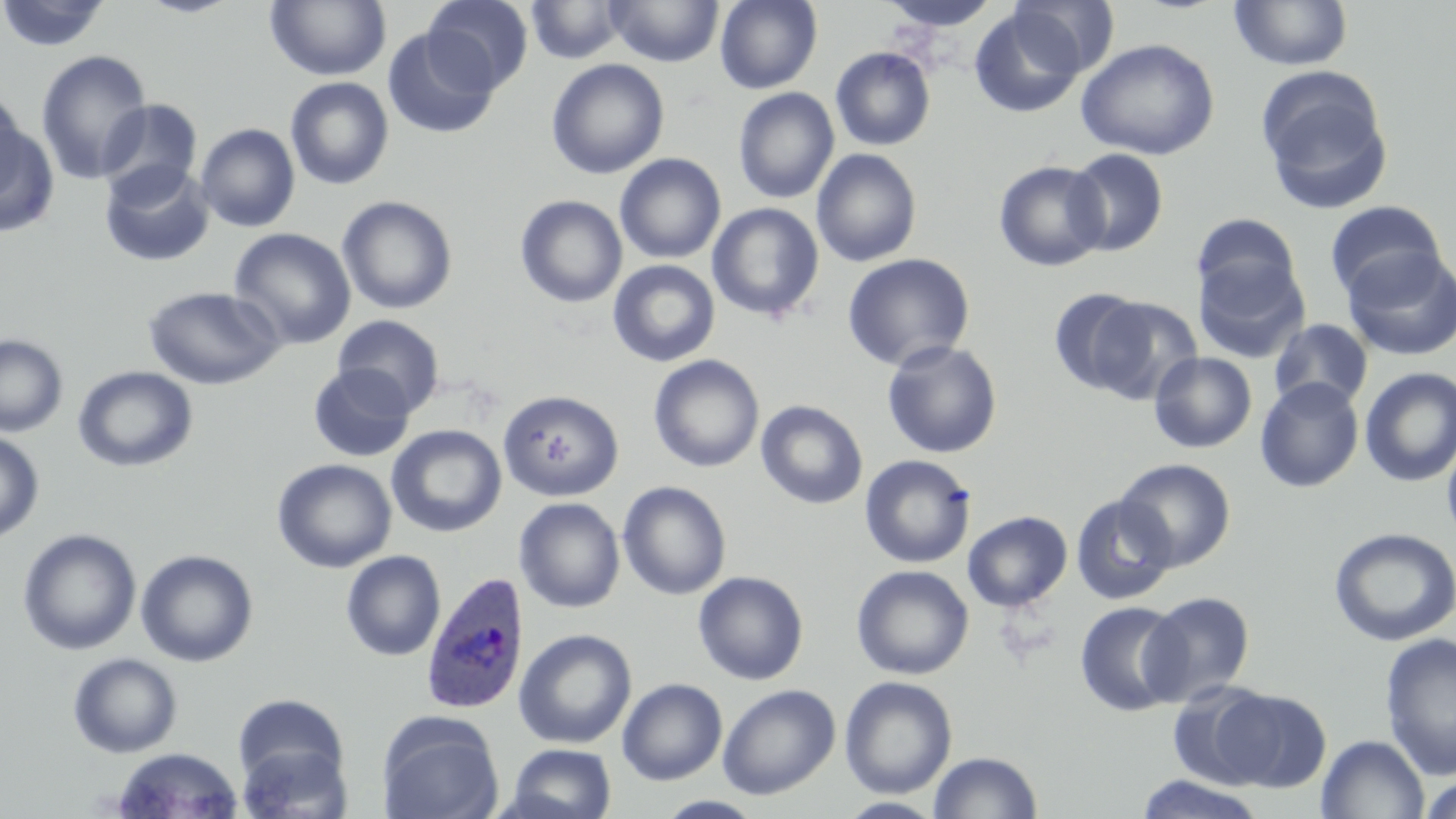

Approximate bounding boxes as (x1, y1, x2, y2) in pixels. Plasmodium ovale-infected red blood cell locations: (420, 570, 529, 714). Uninfected red blood cell locations: (0, 0, 112, 53), (134, 0, 244, 18), (265, 0, 391, 81), (423, 0, 533, 93), (714, 0, 822, 93), (878, 0, 1003, 32), (1010, 0, 1119, 79), (1230, 0, 1353, 71), (526, 1, 629, 64), (606, 1, 724, 67), (968, 5, 1086, 119), (382, 27, 499, 139), (1076, 38, 1220, 161), (830, 47, 936, 151), (36, 51, 153, 184), (546, 58, 669, 179), (1255, 66, 1394, 214), (284, 77, 394, 190), (0, 87, 29, 207), (733, 87, 839, 204), (96, 99, 203, 203), (1, 114, 59, 236), (195, 123, 300, 233), (811, 148, 922, 267), (1064, 148, 1169, 257), (615, 153, 726, 264), (993, 160, 1109, 272), (99, 161, 215, 268), (336, 195, 458, 315), (514, 196, 627, 308), (1325, 200, 1447, 303), (707, 203, 825, 322), (1191, 213, 1303, 310), (229, 227, 356, 349), (1341, 247, 1456, 362), (842, 253, 975, 371), (1193, 253, 1309, 363), (608, 260, 721, 367), (143, 286, 283, 390), (1048, 287, 1152, 395), (1088, 296, 1202, 404), (333, 315, 445, 416), (1268, 318, 1374, 413), (0, 334, 68, 437), (882, 339, 1003, 459), (1149, 352, 1258, 453), (648, 354, 764, 473), (73, 365, 198, 472), (308, 365, 415, 463), (1359, 367, 1456, 488), (1255, 377, 1364, 492), (497, 389, 624, 501), (756, 400, 868, 509), (387, 424, 506, 537), (0, 430, 44, 545), (1441, 430, 1456, 552), (859, 454, 976, 569), (272, 458, 396, 573), (1115, 458, 1237, 571), (617, 481, 731, 600), (1069, 494, 1177, 605), (514, 498, 625, 613), (962, 510, 1073, 612), (1328, 527, 1456, 647), (18, 528, 141, 656), (136, 549, 258, 667), (340, 550, 446, 661), (851, 564, 974, 680), (693, 571, 809, 685), (1141, 591, 1255, 706), (1074, 600, 1188, 717), (514, 628, 637, 749), (1379, 631, 1456, 781), (67, 652, 183, 758), (839, 675, 958, 799), (617, 678, 727, 785), (1167, 680, 1281, 790), (717, 683, 840, 800), (1214, 688, 1332, 792), (234, 694, 350, 794), (376, 713, 504, 819), (1316, 734, 1429, 819), (236, 739, 353, 819), (505, 743, 617, 819), (111, 747, 245, 818), (928, 751, 1043, 818), (1134, 773, 1266, 819), (1419, 774, 1456, 819), (836, 797, 947, 818). Slide-level diagnosis: Plasmodium ovale. One field of a larger specimen. May-Grünwald-Giemsa stain. Optical microscopy. 1000x magnification. Thin blood smear. Image is 1456×819 pixels.